Describe the morphology of the red blood cells.
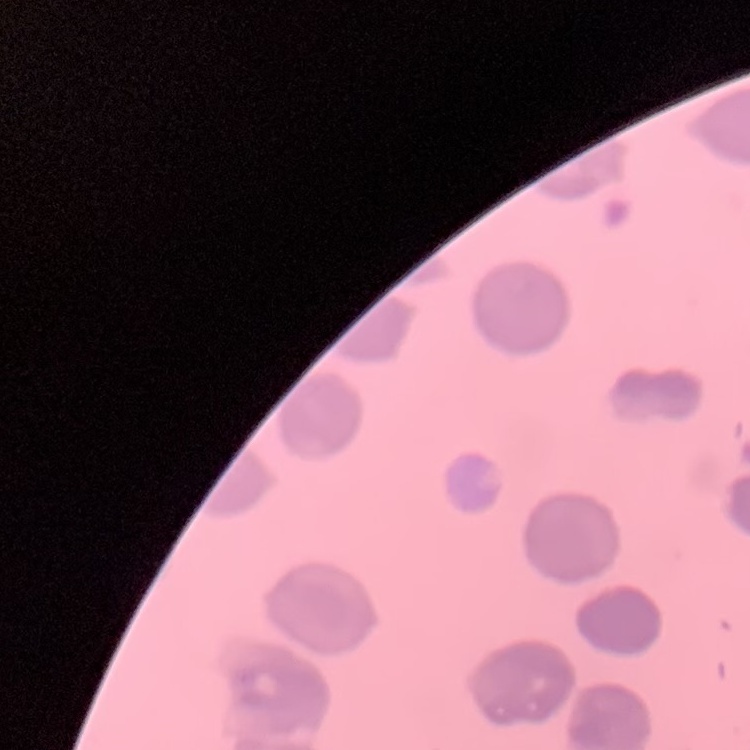
They show no rouleaux formation.

Summary:
  - Image type: square crop of a larger photomicrograph
  - Preparation: thin peripheral smear
  - Stain: Field's or Giemsa